Identify the cell.
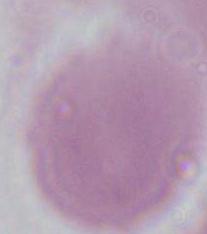

An erythrocyte.

Summary:
  - Modality: photomicrograph
  - Magnification: 1000x